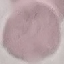
{
  "malaria_status": "uninfected",
  "capture": "smartphone through the microscope eyepiece",
  "preparation": "thin blood smear",
  "image_type": "automatically extracted cell patch, resized to 64 × 64 pixels",
  "stain": "Giemsa"
}